Describe the morphology of the erythrocytes.
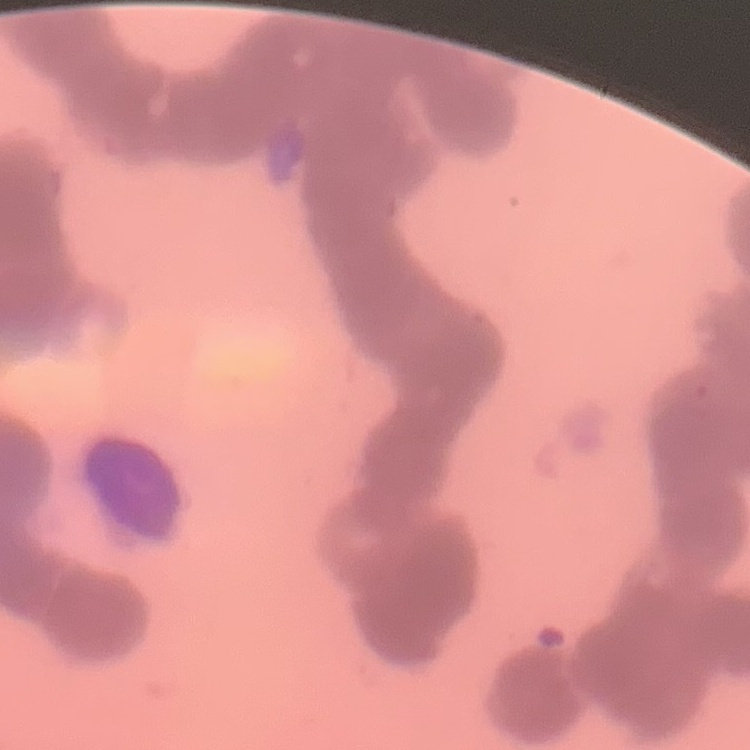

They show rouleaux formation.

Stained with either Field's or Giemsa. Thin peripheral smear. Square crop of a larger photomicrograph.